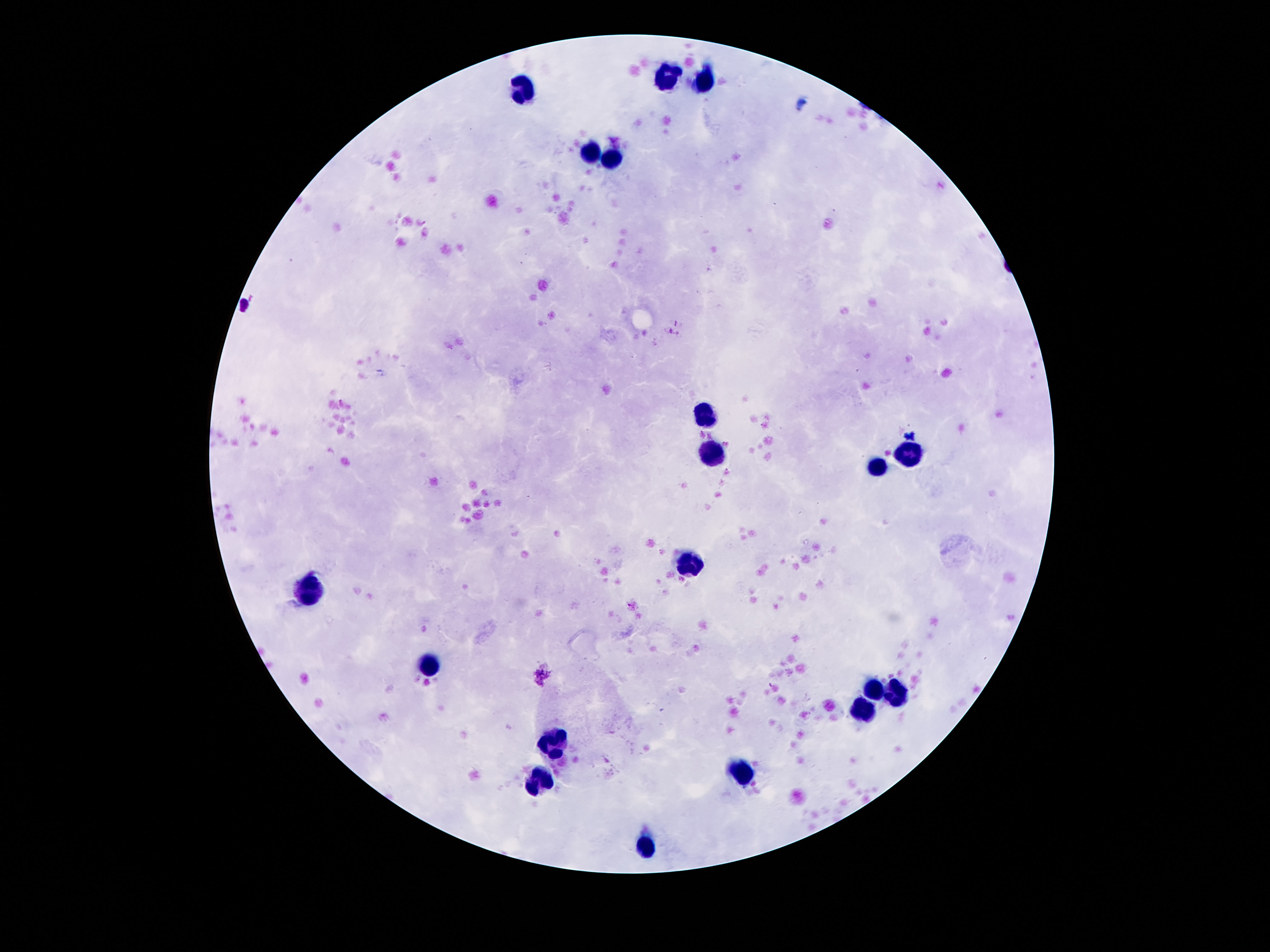

Approximate centers as (x, y) in pixels.
Summary:
  - Leukocyte locations: (669, 78), (707, 80), (520, 90), (589, 155), (610, 156), (705, 414), (707, 452), (910, 455), (878, 467), (692, 563), (313, 593), (425, 665), (875, 690), (897, 698), (863, 711), (557, 739), (744, 772), (537, 782), (647, 849)
  - Preparation: thick blood film
  - Image size: 1270×952 pixels
  - Field of view: one from this slide
  - Patient malaria status: uninfected
  - Magnification: 100x
  - Capture: smartphone camera through the microscope eyepiece
  - Stain: Giemsa